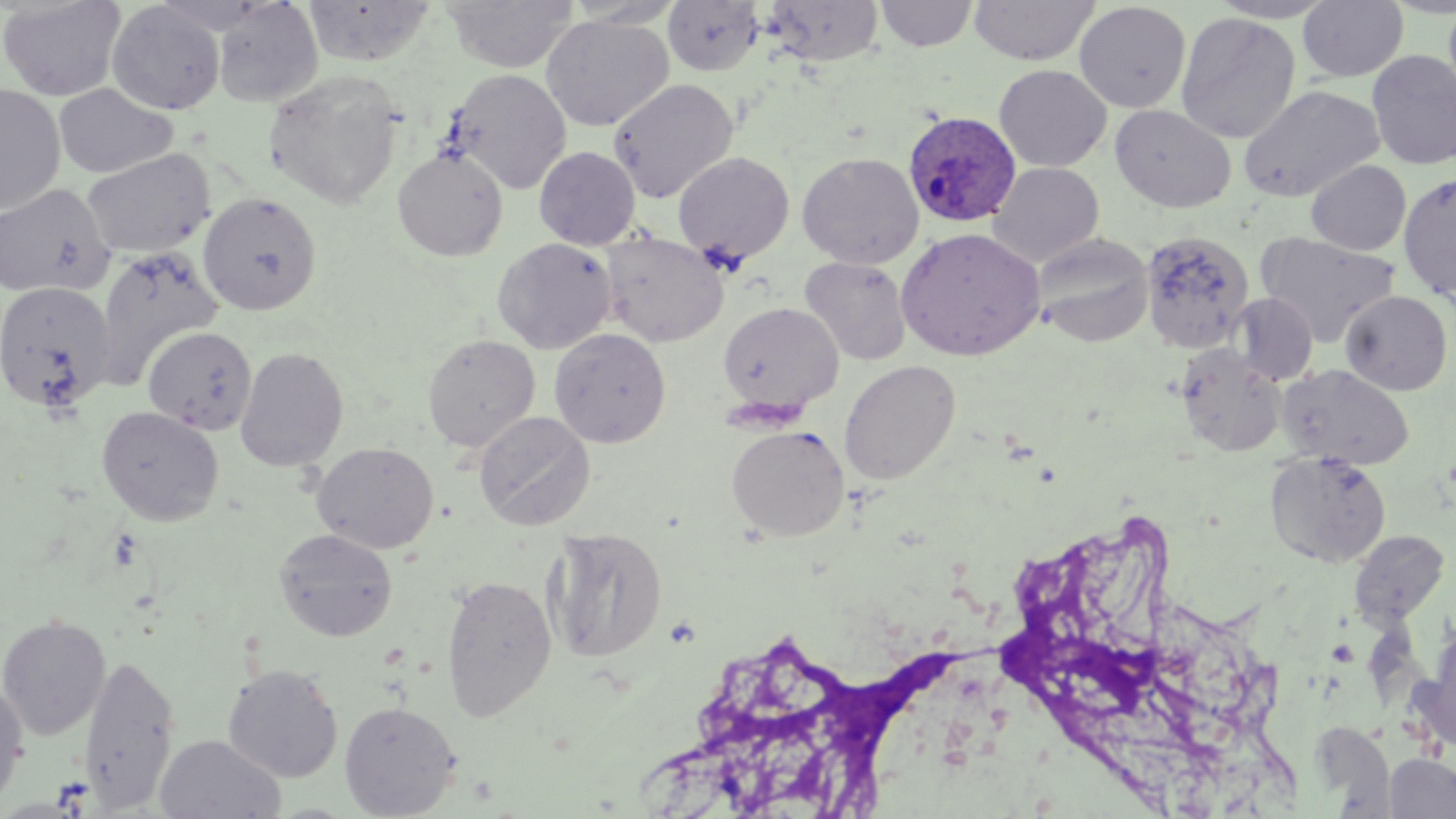

Approximate bounding boxes as [x1, y1, x2, y2] in pixels. Platelet locations: [106, 528, 144, 572]. Plasmodium ovale-infected red blood cell locations: [902, 110, 1022, 228]. Uninfected red blood cell locations: [0, 0, 126, 101], [304, 0, 435, 66], [441, 0, 579, 73], [565, 0, 684, 28], [662, 0, 764, 76], [765, 0, 883, 66], [875, 0, 977, 51], [969, 0, 1099, 65], [1207, 0, 1341, 23], [213, 1, 323, 107], [1297, 1, 1408, 82], [1443, 1, 1456, 104], [106, 2, 225, 115], [1074, 2, 1191, 113], [1176, 12, 1300, 145], [541, 15, 672, 131], [1366, 50, 1456, 170], [993, 64, 1111, 171], [445, 68, 571, 194], [263, 71, 403, 209], [609, 78, 739, 203], [0, 84, 66, 216], [54, 84, 177, 179], [1238, 84, 1385, 202], [1110, 104, 1237, 213], [534, 146, 640, 249], [81, 148, 214, 259], [392, 148, 507, 260], [673, 151, 795, 265], [797, 152, 924, 268], [1306, 160, 1411, 255], [988, 162, 1104, 268], [1398, 172, 1456, 301], [0, 183, 116, 299], [198, 191, 321, 315], [895, 227, 1046, 361], [600, 230, 729, 347], [1142, 230, 1253, 352], [1257, 232, 1399, 345], [1032, 233, 1153, 346], [492, 237, 616, 354], [94, 246, 223, 390], [800, 256, 912, 365], [0, 280, 116, 413], [1340, 290, 1452, 395], [1233, 293, 1318, 386], [718, 302, 844, 413], [142, 326, 257, 435], [549, 328, 671, 448], [422, 333, 541, 453], [1174, 343, 1286, 457], [234, 345, 349, 472], [839, 359, 961, 485], [1278, 364, 1415, 471], [96, 406, 224, 525], [473, 411, 595, 531], [727, 425, 849, 541], [312, 441, 438, 554], [1265, 450, 1392, 568], [547, 526, 668, 663], [273, 528, 398, 641], [1348, 530, 1449, 626], [440, 574, 557, 720], [0, 614, 111, 740], [1417, 632, 1456, 756], [79, 653, 181, 811], [222, 664, 344, 783], [0, 678, 28, 811], [339, 700, 460, 817], [1309, 721, 1395, 813], [154, 733, 286, 818], [1385, 753, 1456, 818]. Slide-level diagnosis: Plasmodium ovale. Optical microscopy. Captured at 1000x magnification. Thin blood smear. May-Grünwald-Giemsa-stained preparation. Single field of view. Image is 1456×819 pixels.